Describe the morphology of the red blood cells.
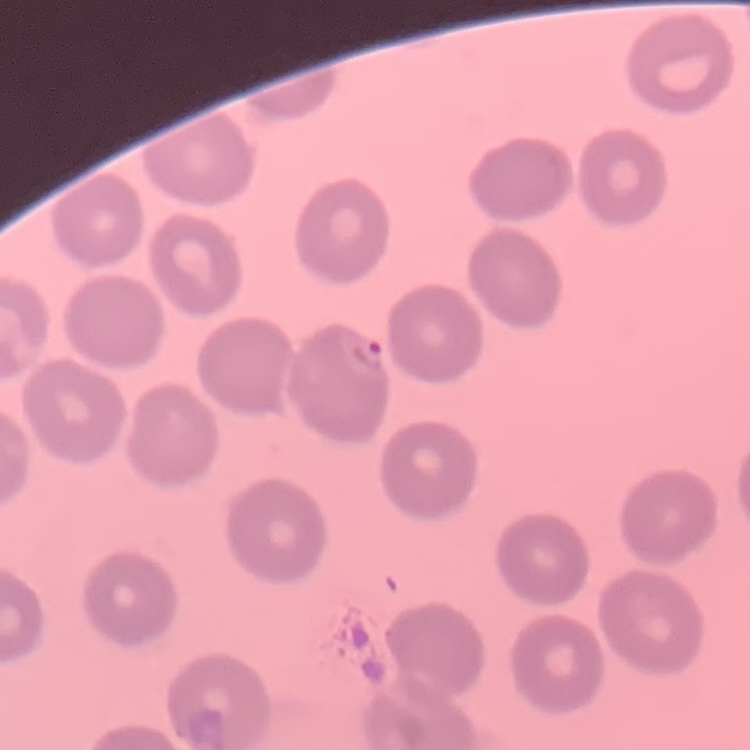

They show no rouleaux formation.

Summary:
  - Image type: one tile cut from a larger photomicrograph
  - Preparation: thin blood smear
  - Stain: Field's or Giemsa